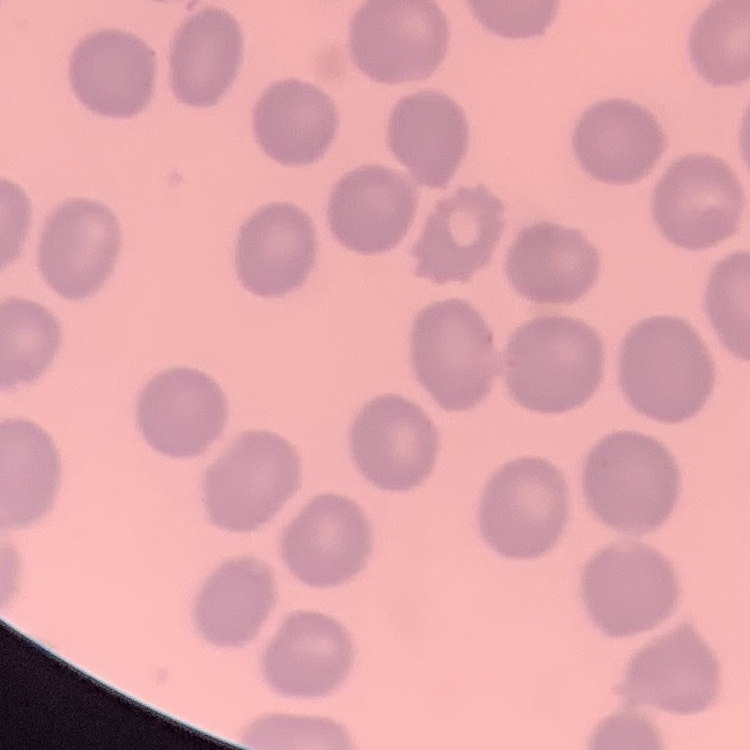
erythrocyte morphology = no rouleaux formation
image type = one tile cut from a larger photomicrograph
stain = Field's or Giemsa
preparation = thin blood smear